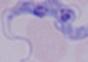

Captured at 1000x magnification. Photomicrograph. A trypanosome is shown.